Identify the blood parasite species.
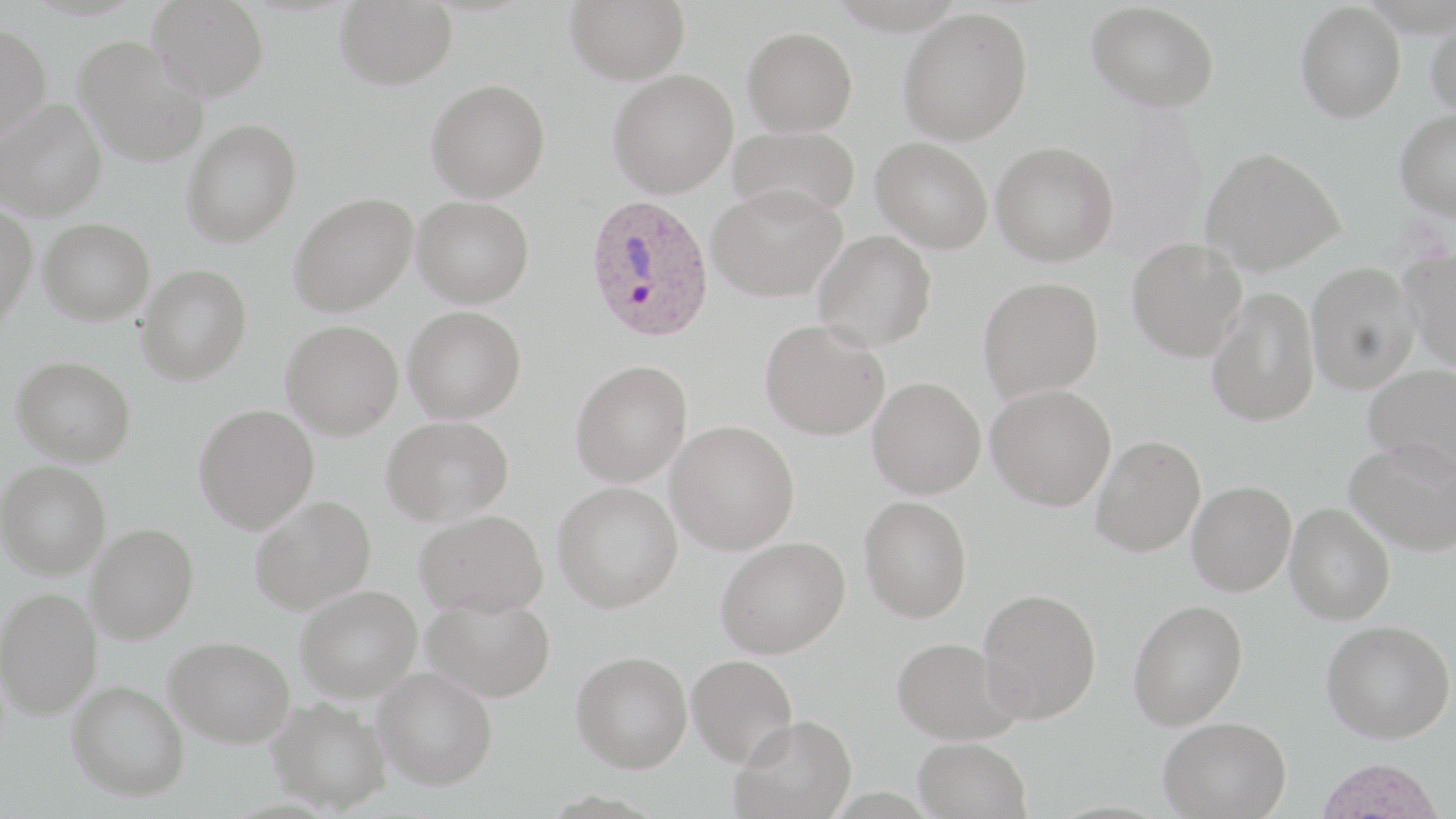

Plasmodium ovale.

Approximate bounding boxes as named x1/y1/x2/y2 corners in pixels. Plasmodium ovale-infected red blood cell locations: (x1=584, y1=194, x2=714, y2=343). Uninfected red blood cell locations: (x1=147, y1=0, x2=269, y2=100), (x1=335, y1=0, x2=457, y2=90), (x1=566, y1=0, x2=689, y2=84), (x1=1087, y1=1, x2=1220, y2=112), (x1=1296, y1=2, x2=1406, y2=122), (x1=898, y1=8, x2=1033, y2=144), (x1=1427, y1=11, x2=1456, y2=118), (x1=0, y1=22, x2=52, y2=143), (x1=742, y1=26, x2=857, y2=136), (x1=74, y1=35, x2=209, y2=167), (x1=607, y1=69, x2=738, y2=198), (x1=426, y1=78, x2=550, y2=202), (x1=1, y1=98, x2=106, y2=221), (x1=1395, y1=109, x2=1456, y2=220), (x1=182, y1=118, x2=302, y2=246), (x1=729, y1=125, x2=861, y2=221), (x1=871, y1=137, x2=993, y2=254), (x1=991, y1=141, x2=1119, y2=266), (x1=1201, y1=147, x2=1344, y2=276), (x1=707, y1=185, x2=846, y2=302), (x1=289, y1=192, x2=418, y2=316), (x1=412, y1=195, x2=534, y2=308), (x1=0, y1=201, x2=38, y2=330), (x1=38, y1=218, x2=154, y2=325), (x1=812, y1=230, x2=937, y2=351), (x1=1127, y1=238, x2=1247, y2=361), (x1=1401, y1=248, x2=1456, y2=371), (x1=1306, y1=259, x2=1419, y2=393), (x1=136, y1=264, x2=252, y2=385), (x1=978, y1=276, x2=1104, y2=401), (x1=1206, y1=287, x2=1320, y2=427), (x1=403, y1=305, x2=526, y2=423), (x1=760, y1=319, x2=891, y2=440), (x1=281, y1=320, x2=403, y2=439), (x1=12, y1=355, x2=136, y2=466), (x1=570, y1=360, x2=692, y2=487), (x1=1363, y1=363, x2=1456, y2=478), (x1=867, y1=377, x2=985, y2=498), (x1=986, y1=384, x2=1116, y2=511), (x1=194, y1=403, x2=319, y2=533), (x1=382, y1=416, x2=514, y2=526), (x1=666, y1=421, x2=799, y2=555), (x1=1090, y1=435, x2=1205, y2=557), (x1=1346, y1=437, x2=1456, y2=555), (x1=0, y1=460, x2=111, y2=579), (x1=553, y1=481, x2=683, y2=612), (x1=1187, y1=481, x2=1296, y2=596), (x1=249, y1=494, x2=376, y2=614), (x1=859, y1=495, x2=972, y2=623), (x1=1285, y1=503, x2=1394, y2=624), (x1=415, y1=509, x2=549, y2=618), (x1=85, y1=522, x2=199, y2=644), (x1=715, y1=536, x2=850, y2=658), (x1=295, y1=584, x2=422, y2=702), (x1=0, y1=586, x2=102, y2=719), (x1=978, y1=588, x2=1102, y2=723), (x1=422, y1=593, x2=556, y2=702), (x1=1128, y1=599, x2=1248, y2=730), (x1=1322, y1=619, x2=1455, y2=743), (x1=165, y1=635, x2=295, y2=746), (x1=891, y1=636, x2=1021, y2=744), (x1=571, y1=650, x2=693, y2=772), (x1=687, y1=653, x2=798, y2=767), (x1=374, y1=666, x2=497, y2=790), (x1=67, y1=680, x2=189, y2=801), (x1=267, y1=696, x2=393, y2=813), (x1=731, y1=715, x2=858, y2=819), (x1=1158, y1=716, x2=1292, y2=818), (x1=913, y1=737, x2=1032, y2=819), (x1=1315, y1=758, x2=1445, y2=819). May-Grünwald-Giemsa-stained preparation. One field of a larger specimen. Image is 1456×819 pixels. Light microscopy. Thin blood smear. Captured at 1000x magnification.